Give the preparation type.
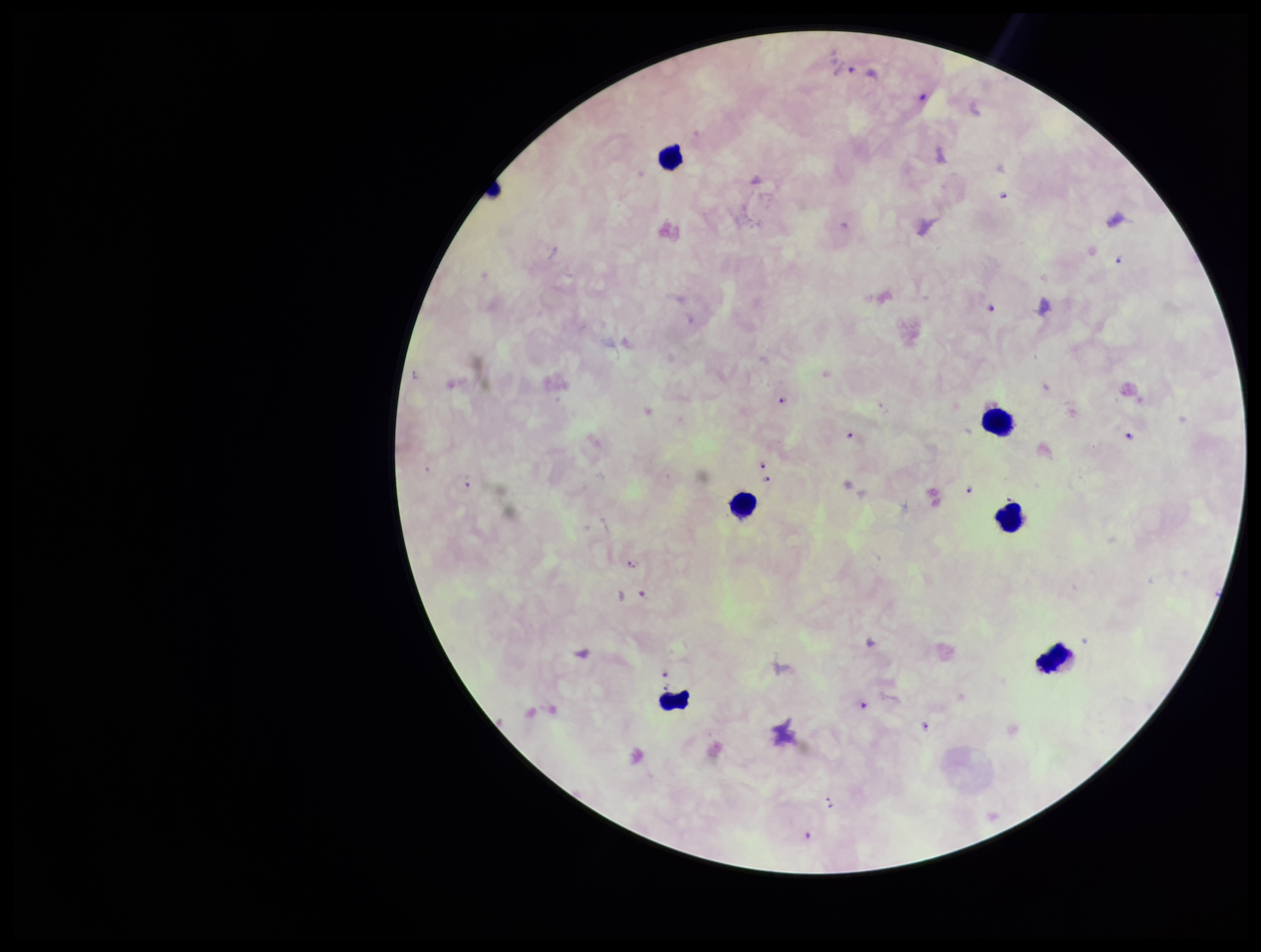
A thick smear.

Species reported for this patient: Plasmodium falciparum. Photographed through the microscope eyepiece with a smartphone camera. Patient malaria status: positive. Parasite count: 15. Image is 1261×952 pixels. Plasmodium parasites: identified. One field from this slide. Giemsa stain. Leukocyte count: 7.